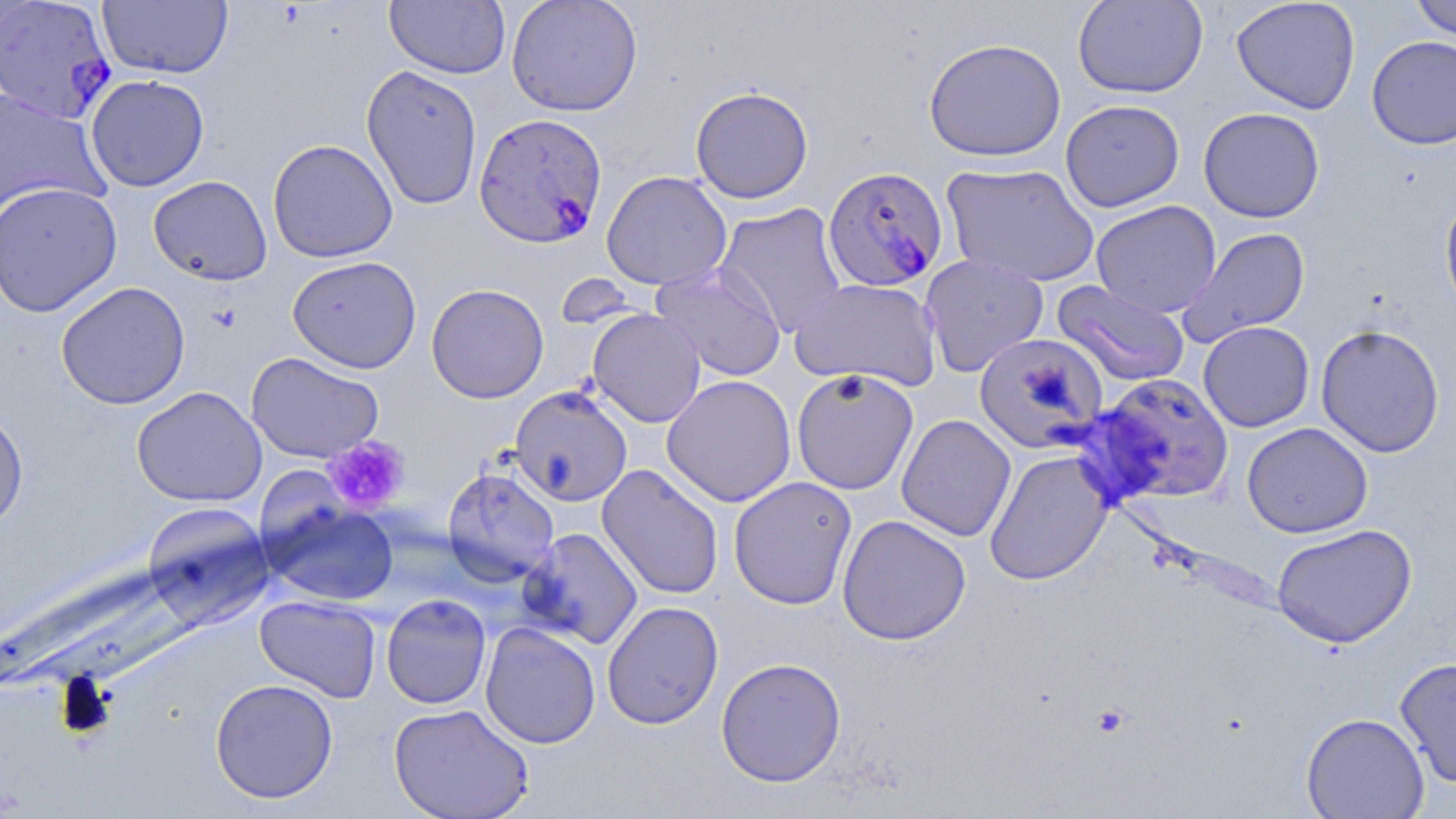
Summary:
  - Coordinate format: approximate bounding boxes as (x1, y1, x2, y2) in pixels
  - Platelet locations: (321, 436, 411, 515)
  - Uninfected red blood cell locations: (385, 0, 511, 79), (506, 0, 642, 116), (1072, 0, 1208, 98), (1230, 0, 1361, 115), (1408, 0, 1456, 40), (98, 1, 233, 79), (1366, 35, 1456, 149), (923, 37, 1067, 162), (360, 65, 483, 211), (85, 74, 210, 192), (690, 86, 814, 203), (0, 90, 109, 219), (1060, 99, 1185, 212), (1198, 107, 1325, 223), (267, 138, 398, 263), (942, 163, 1100, 288), (601, 170, 733, 291), (148, 175, 273, 286), (0, 181, 123, 317), (1439, 191, 1456, 323), (1090, 200, 1221, 318), (714, 203, 848, 337), (1178, 227, 1311, 346), (919, 254, 1049, 377), (287, 255, 421, 373), (651, 264, 787, 381), (789, 277, 942, 392), (1052, 280, 1190, 387), (56, 281, 191, 410), (426, 283, 548, 404), (588, 308, 706, 428), (1198, 321, 1315, 432), (1315, 323, 1445, 458), (973, 332, 1108, 453), (245, 352, 384, 463), (791, 369, 919, 495), (1091, 373, 1235, 504), (661, 374, 797, 507), (131, 385, 267, 507), (510, 386, 633, 506), (0, 406, 29, 536), (896, 413, 1017, 542), (1242, 422, 1373, 538), (984, 450, 1113, 586), (596, 464, 725, 600), (441, 466, 560, 586), (728, 476, 858, 610), (261, 499, 400, 607), (141, 502, 275, 629), (836, 514, 972, 646), (1271, 523, 1417, 649), (518, 527, 644, 649), (380, 593, 492, 709), (255, 594, 382, 703), (601, 600, 724, 730), (480, 622, 601, 749), (1395, 656, 1456, 788), (715, 657, 847, 788), (209, 678, 339, 803), (388, 702, 534, 819), (1301, 712, 1429, 819)
  - Plasmodium falciparum-infected red blood cell locations: (0, 1, 118, 124), (473, 112, 608, 249), (823, 165, 949, 293)
  - Slide-level diagnosis: Plasmodium falciparum
  - Preparation: thin blood smear
  - Modality: optical microscopy
  - Field of view: one of a larger specimen
  - Image size: 1456×819 pixels
  - Stain: May-Grünwald-Giemsa
  - Magnification: 1000x